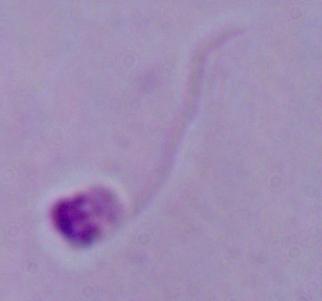

modality = photomicrograph
identification = Leishmania
magnification = 1000x